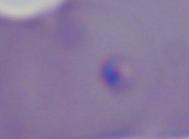
magnification = 1000x
identification = Babesia
modality = micrograph